Classify this cell by malaria status.
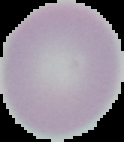

It is uninfected.

The area outside the segmented cell region is set to black. Image is 124×142 pixels. From a thin blood smear.